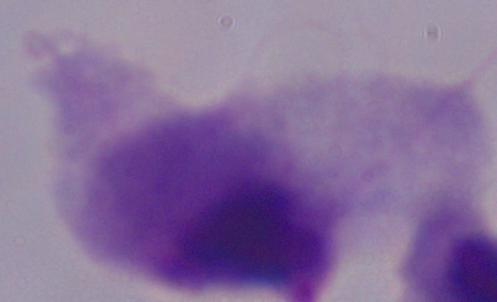
identification = trichomonad
magnification = 1000x
modality = micrograph